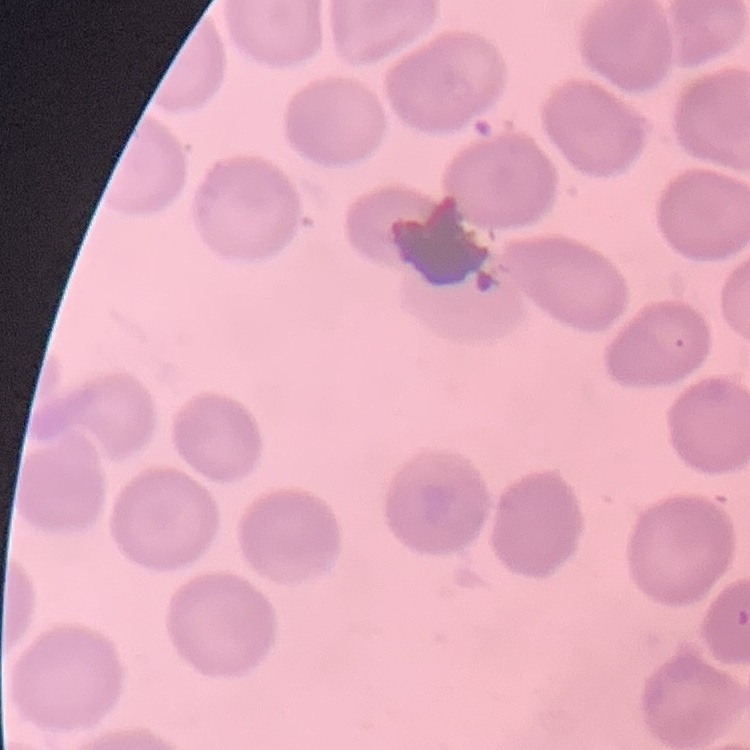

Summary:
  - Erythrocyte morphology: no rouleaux formation
  - Image type: square crop of a larger photomicrograph
  - Preparation: thin peripheral smear
  - Stain: Field's or Giemsa